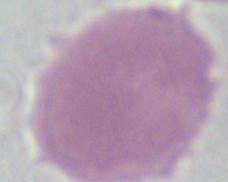
identification = erythrocyte
modality = micrograph
magnification = 1000x